Comment on the morphology of the red blood cells.
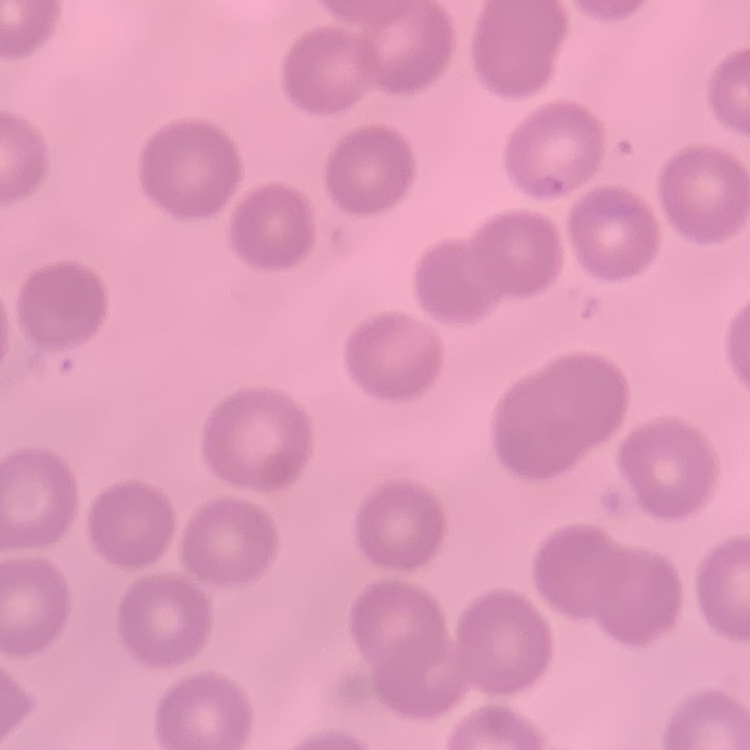
They show no rouleaux formation.

stain: Field's or Giemsa
preparation: thin peripheral smear
image_type: square crop of a larger photomicrograph